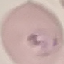

malaria_status: parasitized
image_type: cell patch, automatically extracted from a larger field of view and resized to 64 × 64 pixels
stain: Giemsa
capture: smartphone through the microscope eyepiece
preparation: thin blood smear